Report the malaria status of this cell.
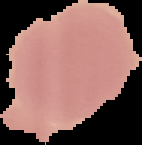

It is uninfected.

Summary:
  - Image type: cell region segmented out of the field of view; surrounding area masked to black
  - Image size: 142×145 pixels
  - Preparation: thin blood smear